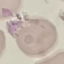
{
  "malaria_status": "uninfected",
  "capture": "smartphone through the microscope eyepiece",
  "image_type": "cell patch, automatically extracted from a larger field of view and resized to 64 × 64 pixels",
  "preparation": "thin blood film",
  "stain": "Giemsa"
}